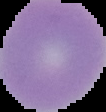

The area outside the segmented cell region is set to black. Image is 106×112 pixels. From a thin blood smear. Result: no Plasmodium parasites detected.